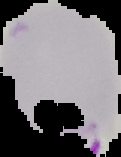

Summary:
  - Image size: 121×157 pixels
  - Malaria status: parasitized
  - Preparation: thin blood film
  - Image type: cell region segmented out of the field of view; surrounding area masked to black